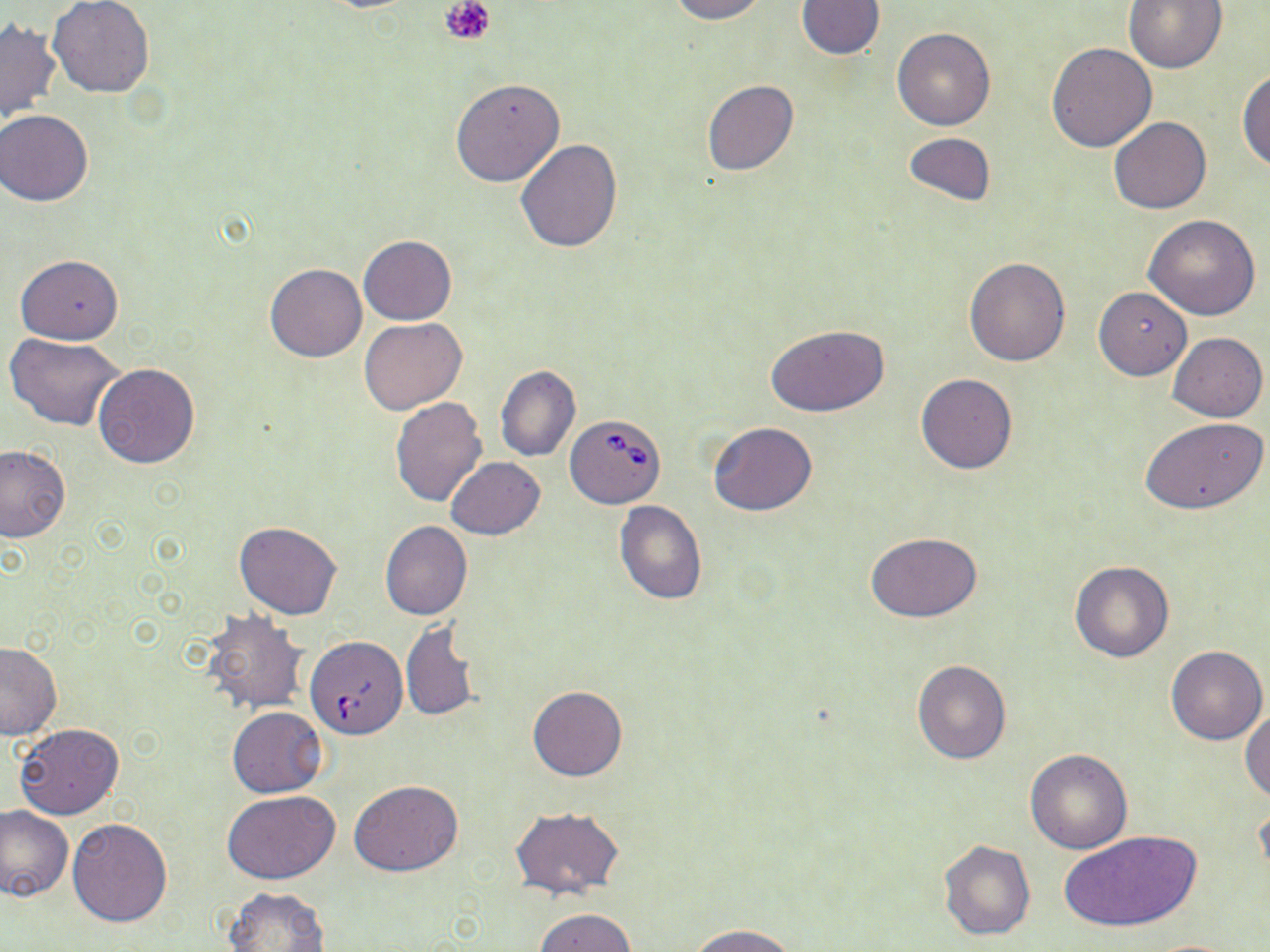
slide-level diagnosis = Babesia divergens
uninfected red blood cell locations = approximate bounding boxes as named x1/y1/x2/y2 corners in pixels: (x1=668, y1=0, x2=768, y2=23), (x1=796, y1=0, x2=886, y2=60), (x1=48, y1=1, x2=154, y2=99), (x1=1123, y1=1, x2=1226, y2=73), (x1=0, y1=19, x2=61, y2=124), (x1=892, y1=26, x2=996, y2=131), (x1=1046, y1=42, x2=1157, y2=152), (x1=1237, y1=67, x2=1270, y2=172), (x1=450, y1=77, x2=565, y2=188), (x1=702, y1=80, x2=797, y2=176), (x1=1, y1=110, x2=93, y2=205), (x1=1108, y1=117, x2=1213, y2=214), (x1=902, y1=132, x2=996, y2=207), (x1=514, y1=138, x2=622, y2=253), (x1=1144, y1=213, x2=1261, y2=319), (x1=359, y1=235, x2=456, y2=324), (x1=15, y1=253, x2=124, y2=343), (x1=964, y1=256, x2=1070, y2=367), (x1=263, y1=264, x2=366, y2=362), (x1=1094, y1=287, x2=1192, y2=380), (x1=359, y1=317, x2=466, y2=415), (x1=765, y1=324, x2=891, y2=417), (x1=5, y1=332, x2=126, y2=431), (x1=1167, y1=332, x2=1267, y2=421), (x1=92, y1=363, x2=200, y2=469), (x1=496, y1=365, x2=581, y2=463), (x1=915, y1=373, x2=1018, y2=474), (x1=390, y1=396, x2=487, y2=506), (x1=1140, y1=416, x2=1268, y2=515), (x1=709, y1=423, x2=817, y2=516), (x1=0, y1=444, x2=70, y2=542), (x1=446, y1=457, x2=545, y2=540), (x1=614, y1=501, x2=708, y2=604), (x1=233, y1=521, x2=342, y2=620), (x1=380, y1=521, x2=472, y2=619), (x1=864, y1=530, x2=984, y2=623), (x1=1068, y1=559, x2=1174, y2=663), (x1=201, y1=609, x2=308, y2=714), (x1=401, y1=621, x2=481, y2=721), (x1=0, y1=641, x2=61, y2=739), (x1=1165, y1=645, x2=1267, y2=745), (x1=912, y1=659, x2=1010, y2=764), (x1=528, y1=686, x2=627, y2=781), (x1=226, y1=707, x2=328, y2=798), (x1=1241, y1=708, x2=1270, y2=801), (x1=14, y1=722, x2=124, y2=821), (x1=1025, y1=748, x2=1133, y2=854), (x1=350, y1=780, x2=463, y2=877), (x1=223, y1=790, x2=340, y2=883), (x1=1255, y1=798, x2=1270, y2=888), (x1=0, y1=805, x2=74, y2=901), (x1=510, y1=807, x2=624, y2=900), (x1=68, y1=817, x2=173, y2=926), (x1=1058, y1=831, x2=1199, y2=933), (x1=938, y1=839, x2=1035, y2=940), (x1=224, y1=886, x2=331, y2=951), (x1=535, y1=907, x2=636, y2=952), (x1=689, y1=924, x2=797, y2=952), (x1=1141, y1=938, x2=1243, y2=951)
Babesia divergens-infected red blood cell locations = approximate bounding boxes as named x1/y1/x2/y2 corners in pixels: (x1=566, y1=413, x2=665, y2=507), (x1=305, y1=636, x2=407, y2=739)
field of view = one of a larger specimen
modality = optical microscopy
stain = May-Grünwald-Giemsa
image size = 1270×952 pixels
preparation = thin blood film
platelet locations = approximate bounding boxes as named x1/y1/x2/y2 corners in pixels: (x1=440, y1=0, x2=497, y2=45)
magnification = 1000x